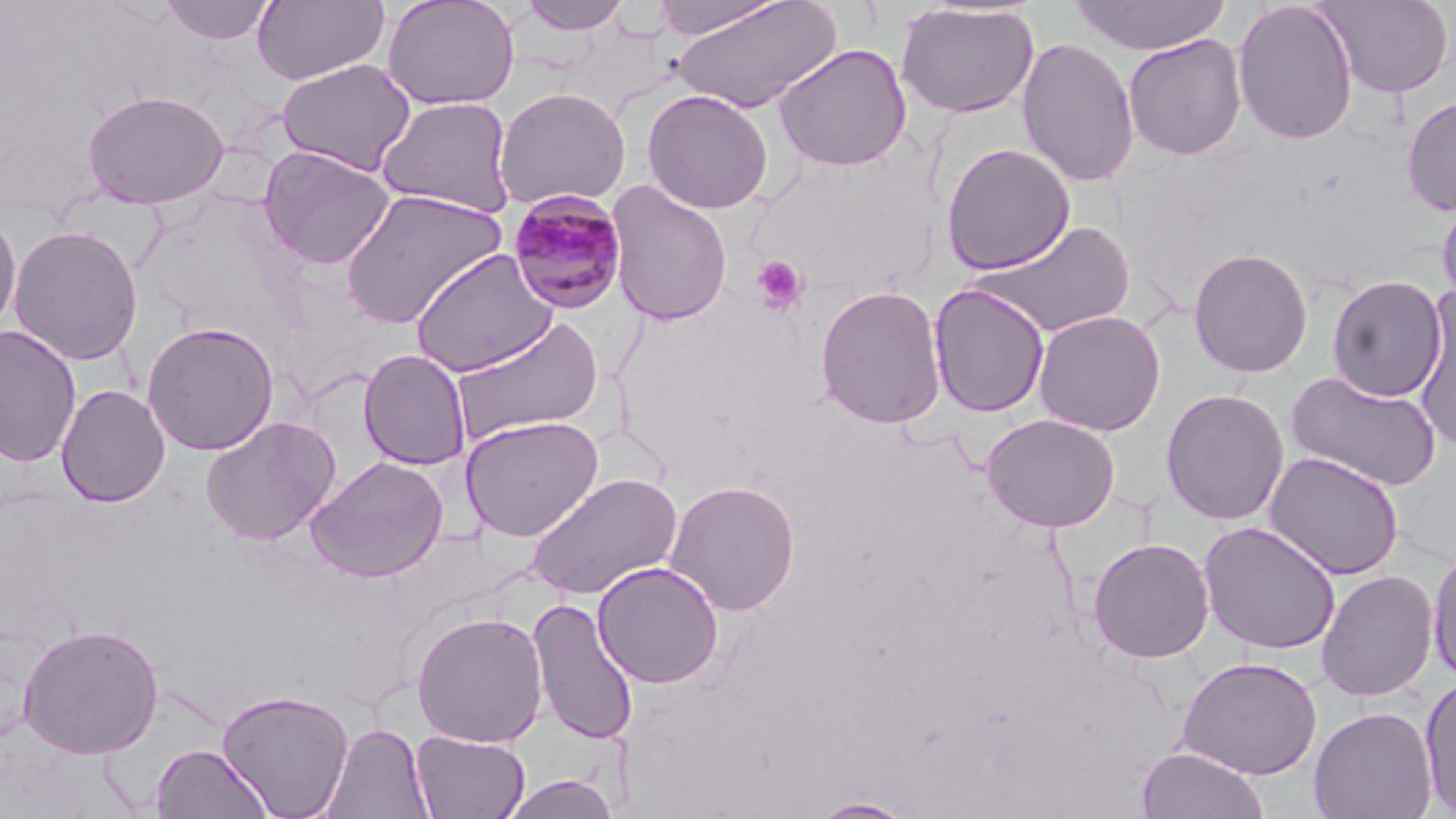

{
  "slide_level_diagnosis": "Plasmodium malariae",
  "platelet_locations": "approximate bounding boxes as [x1, y1, x2, y2] in pixels: [751, 255, 809, 315]",
  "magnification": "1000x",
  "preparation": "thin blood smear",
  "stain": "May-Grünwald-Giemsa",
  "uninfected_red_blood_cell_locations": "approximate bounding boxes as [x1, y1, x2, y2] in pixels: [158, 0, 276, 45], [252, 0, 389, 85], [382, 0, 519, 111], [516, 0, 634, 36], [668, 0, 842, 113], [1069, 0, 1232, 55], [1317, 0, 1455, 98], [1232, 1, 1359, 146], [894, 3, 1039, 119], [1123, 34, 1247, 160], [1016, 36, 1140, 188], [773, 43, 912, 172], [276, 58, 417, 176], [493, 86, 631, 211], [82, 89, 230, 209], [640, 89, 775, 214], [1401, 94, 1456, 216], [376, 96, 516, 217], [749, 142, 942, 301], [941, 142, 1076, 274], [258, 146, 395, 269], [605, 180, 733, 327], [339, 188, 508, 329], [1436, 189, 1456, 319], [0, 206, 22, 338], [970, 218, 1137, 339], [8, 224, 144, 365], [1188, 247, 1313, 378], [410, 250, 558, 377], [1327, 275, 1448, 403], [930, 283, 1050, 418], [814, 284, 948, 430], [1411, 288, 1456, 450], [1032, 309, 1166, 437], [448, 315, 606, 444], [142, 321, 279, 456], [0, 324, 82, 468], [358, 349, 472, 470], [1285, 370, 1442, 492], [56, 384, 171, 507], [1160, 388, 1290, 525], [982, 413, 1121, 532], [201, 415, 341, 545], [459, 415, 605, 542], [1264, 450, 1405, 581], [305, 455, 449, 583], [526, 472, 683, 600], [664, 480, 801, 616], [1198, 521, 1341, 655], [1087, 537, 1215, 664], [1427, 545, 1456, 686], [591, 561, 724, 688], [1316, 568, 1438, 702], [526, 597, 639, 746], [410, 610, 548, 748], [16, 623, 164, 759], [1176, 656, 1323, 780], [1418, 673, 1456, 814], [217, 688, 355, 818], [1308, 706, 1437, 819], [322, 722, 434, 819], [411, 730, 530, 818], [150, 743, 273, 818], [1136, 746, 1269, 819], [498, 773, 621, 819], [808, 797, 917, 818]",
  "modality": "optical microscopy",
  "image_size": "1456×819 pixels",
  "field_of_view": "single",
  "plasmodium_malariae_infected_red_blood_cell_locations": "approximate bounding boxes as [x1, y1, x2, y2] in pixels: [506, 190, 629, 314]"
}